Report the malaria status of this cell.
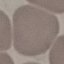

It is uninfected.

{
  "preparation": "thin blood film",
  "capture": "smartphone through the microscope eyepiece",
  "stain": "Giemsa",
  "image_type": "cell patch, automatically extracted from a larger field of view and resized to 64 × 64 pixels"
}